Assess this cell for malaria.
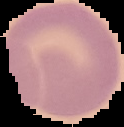

It is uninfected.

image type = cell region segmented out of the field of view; surrounding area masked to black
preparation = thin blood film
image size = 124×127 pixels